Point out each Plasmodium parasite.
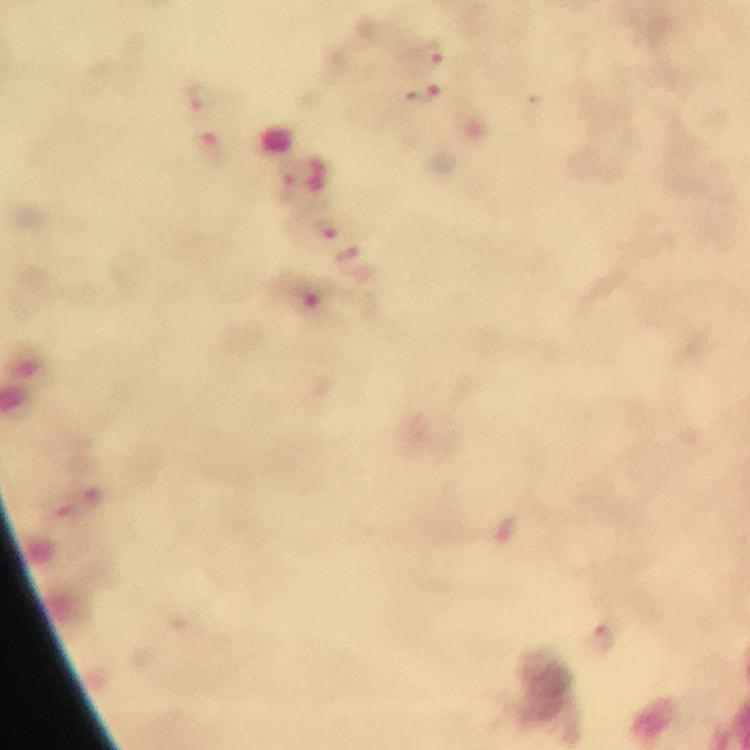

Approximate centers as [x, y] in pixels.
Plasmodium parasites: [428, 53], [422, 97], [198, 99], [210, 149], [285, 189], [329, 228], [598, 638].

immersion oil = applied
magnification = 100x
preparation = thick blood smear
capture = smartphone camera through the microscope
context = from a diagnostic examination for malaria
stain = Giemsa
image size = 750×750 pixels
cropped from = one field of view